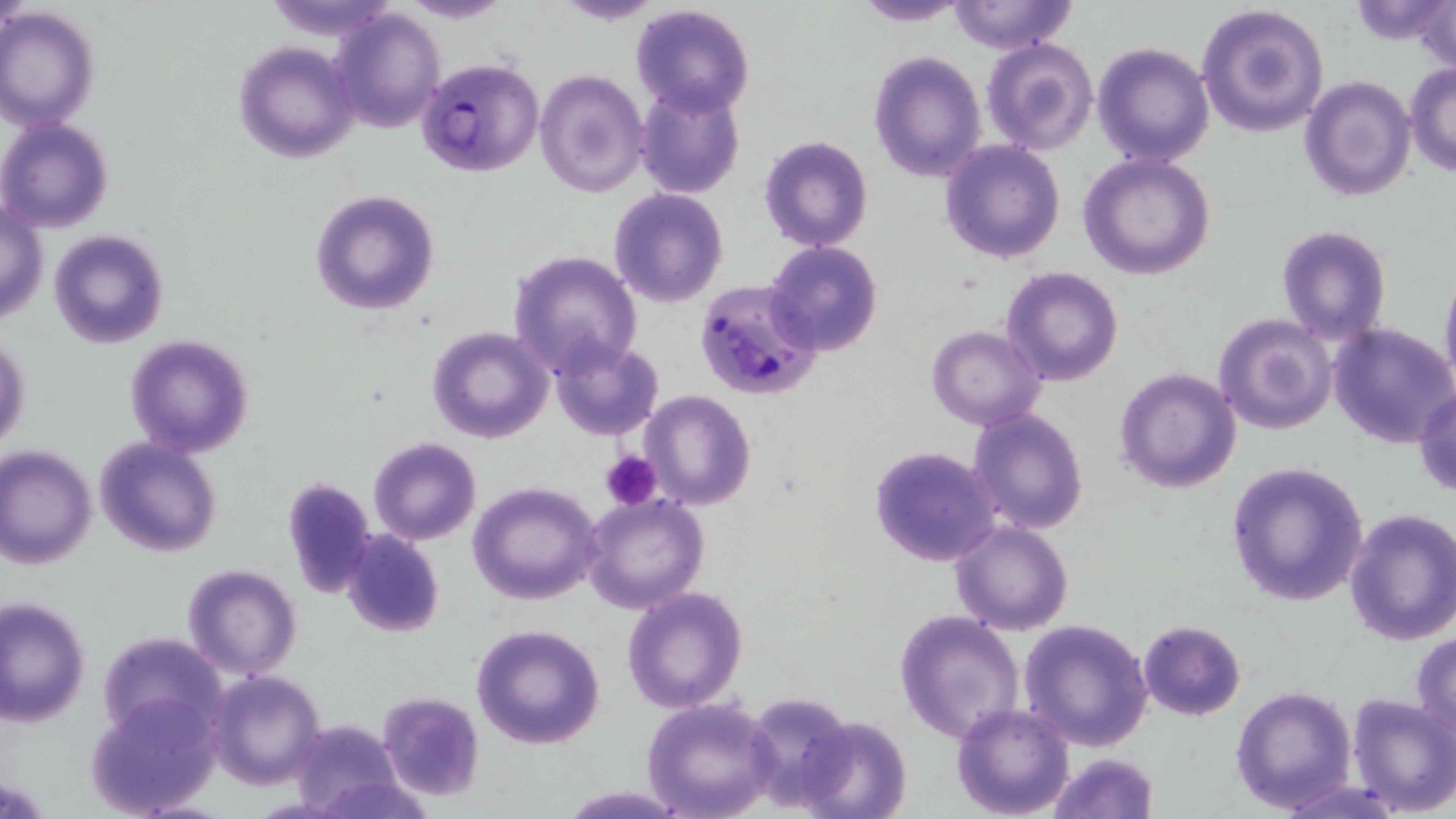
Approximate bounding boxes as named x1/y1/x2/y2 corners in pixels. Uninfected red blood cell locations: (x1=263, y1=0, x2=404, y2=40), (x1=400, y1=0, x2=515, y2=23), (x1=552, y1=0, x2=667, y2=26), (x1=944, y1=0, x2=1077, y2=54), (x1=1345, y1=0, x2=1451, y2=46), (x1=1413, y1=0, x2=1454, y2=76), (x1=851, y1=1, x2=971, y2=25), (x1=0, y1=2, x2=29, y2=33), (x1=629, y1=2, x2=755, y2=117), (x1=1195, y1=3, x2=1329, y2=137), (x1=0, y1=7, x2=99, y2=130), (x1=329, y1=7, x2=446, y2=133), (x1=981, y1=37, x2=1099, y2=156), (x1=233, y1=40, x2=360, y2=165), (x1=1091, y1=42, x2=1215, y2=167), (x1=869, y1=52, x2=987, y2=182), (x1=1404, y1=63, x2=1456, y2=176), (x1=534, y1=69, x2=650, y2=196), (x1=1299, y1=75, x2=1417, y2=203), (x1=634, y1=83, x2=744, y2=200), (x1=0, y1=117, x2=114, y2=234), (x1=759, y1=135, x2=873, y2=251), (x1=939, y1=138, x2=1066, y2=262), (x1=1079, y1=153, x2=1216, y2=281), (x1=308, y1=188, x2=440, y2=314), (x1=607, y1=188, x2=729, y2=309), (x1=1, y1=201, x2=48, y2=327), (x1=1274, y1=224, x2=1393, y2=346), (x1=48, y1=229, x2=168, y2=350), (x1=764, y1=240, x2=883, y2=357), (x1=507, y1=248, x2=643, y2=376), (x1=1001, y1=267, x2=1124, y2=386), (x1=1439, y1=267, x2=1456, y2=391), (x1=1212, y1=312, x2=1337, y2=435), (x1=1328, y1=321, x2=1456, y2=449), (x1=927, y1=325, x2=1046, y2=430), (x1=426, y1=326, x2=553, y2=444), (x1=1, y1=333, x2=30, y2=454), (x1=123, y1=334, x2=255, y2=459), (x1=550, y1=338, x2=664, y2=440), (x1=1114, y1=367, x2=1241, y2=495), (x1=1413, y1=384, x2=1456, y2=497), (x1=639, y1=391, x2=757, y2=511), (x1=968, y1=408, x2=1089, y2=534), (x1=93, y1=437, x2=222, y2=557), (x1=366, y1=437, x2=483, y2=546), (x1=0, y1=445, x2=97, y2=569), (x1=867, y1=445, x2=1003, y2=568), (x1=1225, y1=460, x2=1369, y2=607), (x1=280, y1=476, x2=377, y2=598), (x1=467, y1=481, x2=602, y2=605), (x1=581, y1=492, x2=711, y2=614), (x1=1343, y1=508, x2=1456, y2=646), (x1=949, y1=520, x2=1075, y2=636), (x1=340, y1=530, x2=445, y2=638), (x1=182, y1=564, x2=302, y2=680), (x1=623, y1=587, x2=749, y2=713), (x1=1, y1=596, x2=90, y2=726), (x1=893, y1=609, x2=1024, y2=746), (x1=1017, y1=618, x2=1154, y2=753), (x1=1138, y1=619, x2=1246, y2=720), (x1=470, y1=624, x2=606, y2=749), (x1=98, y1=632, x2=225, y2=741), (x1=1411, y1=632, x2=1456, y2=743), (x1=206, y1=669, x2=325, y2=788), (x1=1231, y1=685, x2=1358, y2=813), (x1=742, y1=689, x2=856, y2=810), (x1=85, y1=692, x2=223, y2=816), (x1=375, y1=692, x2=485, y2=801), (x1=1346, y1=694, x2=1456, y2=816), (x1=642, y1=698, x2=780, y2=818), (x1=953, y1=703, x2=1075, y2=818), (x1=794, y1=715, x2=912, y2=819), (x1=293, y1=719, x2=404, y2=818), (x1=1044, y1=753, x2=1161, y2=819), (x1=305, y1=771, x2=431, y2=819), (x1=558, y1=785, x2=691, y2=817). Plasmodium falciparum-infected red blood cell locations: (x1=415, y1=57, x2=544, y2=178), (x1=696, y1=280, x2=822, y2=402). Platelet locations: (x1=602, y1=449, x2=660, y2=510). Slide-level diagnosis: Plasmodium falciparum. One field of a larger specimen. Thin blood film. Light microscopy. May-Grünwald-Giemsa-stained preparation. Image is 1456×819 pixels. 1000x magnification.